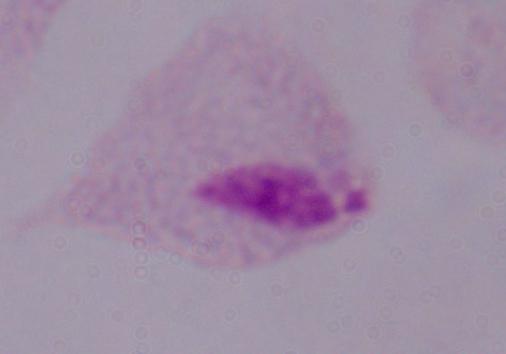

{
  "modality": "micrograph",
  "identification": "trichomonad",
  "magnification": "1000x"
}